Report the malaria status of this cell.
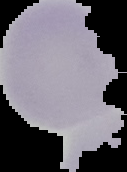

It is uninfected.

Summary:
  - Preparation: thin blood smear
  - Image type: segmented cell region with the area outside set to black
  - Image size: 127×172 pixels